Give the position of every leukocyte.
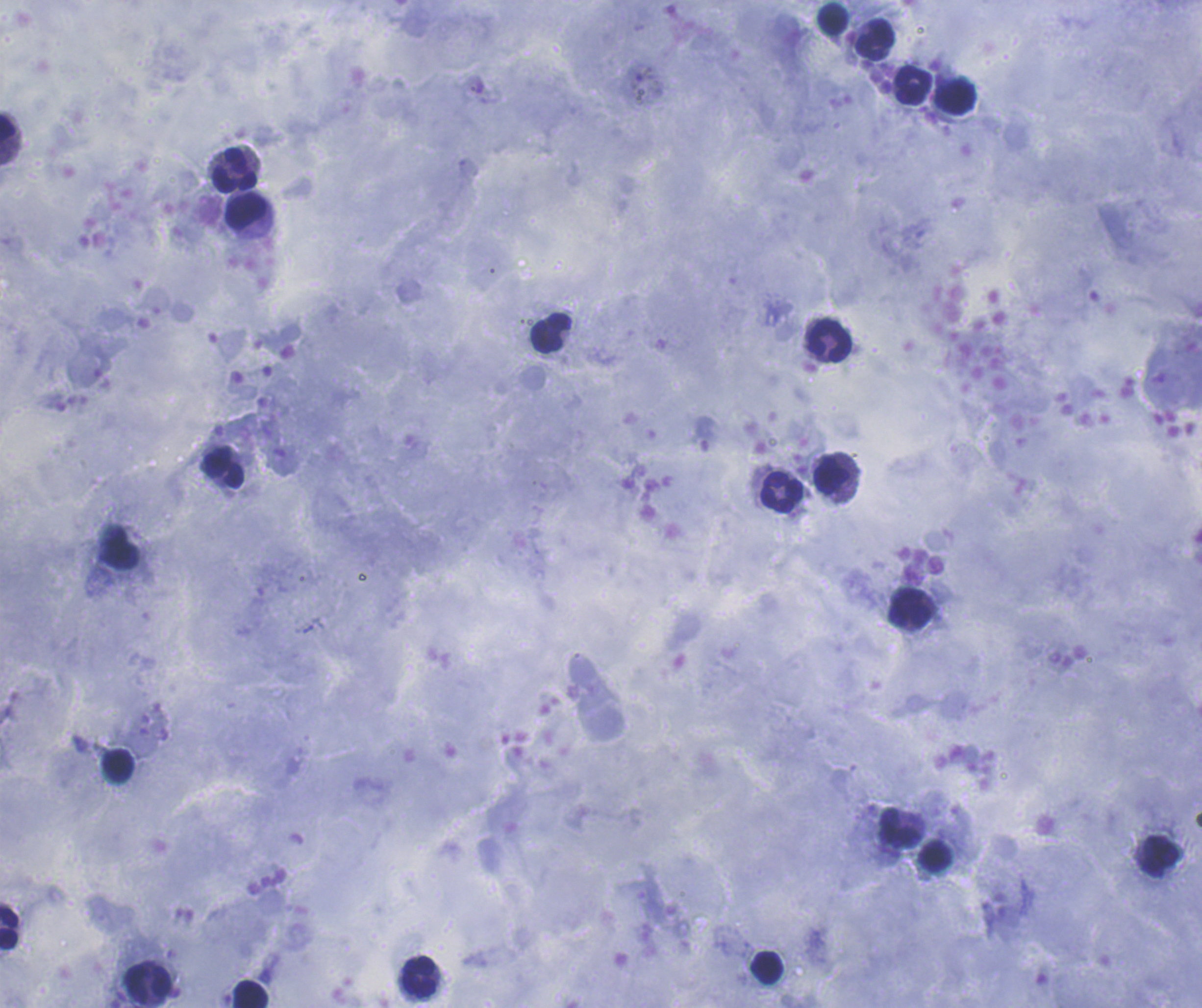

Approximate object centers, in pixels from the top-left corner.
Leukocytes: (x=834, y=18), (x=876, y=39), (x=914, y=85), (x=957, y=98), (x=7, y=130), (x=235, y=170), (x=247, y=213), (x=551, y=333), (x=830, y=341), (x=223, y=468), (x=832, y=476), (x=781, y=492), (x=119, y=548), (x=910, y=609), (x=119, y=765), (x=899, y=828), (x=935, y=855), (x=1159, y=855), (x=9, y=927), (x=767, y=967), (x=419, y=976), (x=148, y=982), (x=249, y=995).

Summary:
  - Image size: 1202×1008 pixels
  - Stain: Romanowsky
  - Background quality: satisfactory
  - Context: previously used in a real diagnosis
  - Coloration quality: good
  - Preparation: thick smear of blood
  - Magnification: 100x
  - Field of view: single
  - Result: no Plasmodium parasites seen